Locate every leukocyte (white blood cell).
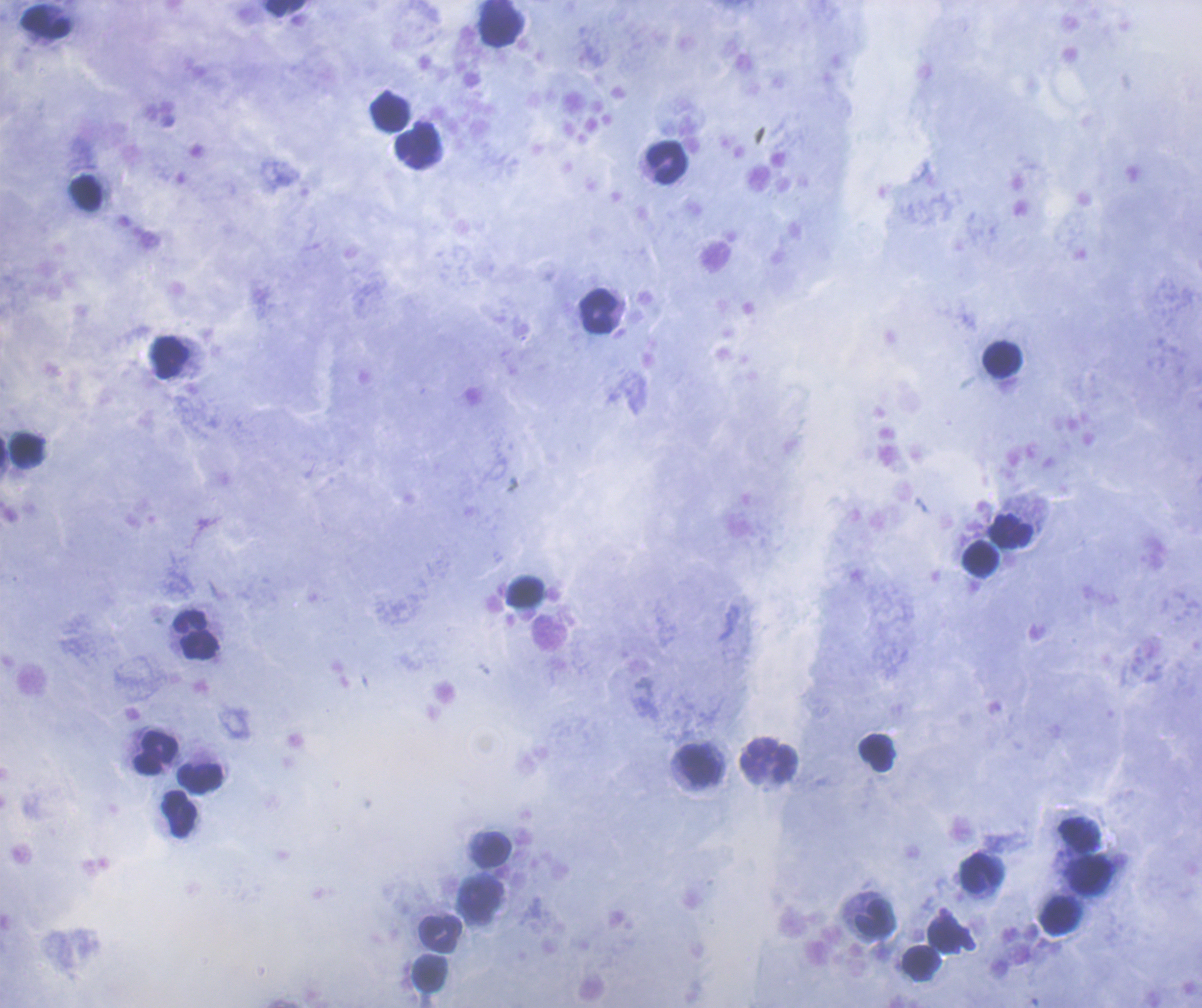

Approximate object centers, in pixels from the top-left corner.
Leukocytes: (x=285, y=9), (x=47, y=23), (x=501, y=23), (x=389, y=112), (x=417, y=147), (x=667, y=162), (x=86, y=194), (x=598, y=311), (x=170, y=357), (x=1003, y=358), (x=27, y=449), (x=1011, y=532), (x=981, y=559), (x=525, y=592), (x=197, y=634), (x=876, y=752), (x=156, y=753), (x=770, y=761), (x=700, y=766), (x=200, y=778), (x=179, y=814), (x=1080, y=836), (x=492, y=849), (x=981, y=872), (x=1091, y=876), (x=483, y=900), (x=1061, y=916), (x=876, y=918), (x=441, y=933), (x=946, y=936), (x=921, y=963), (x=429, y=973).

Result: no Plasmodium parasites detected. Image is 1202×1008 pixels. One field from this slide. Previously used in an actual diagnosis. Coloration quality: good. Thick blood film. 100x magnification. Romanowsky-stained preparation. Background quality: satisfactory.